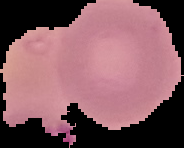

{
  "preparation": "thin blood film",
  "result": "no malaria parasites detected",
  "image_size": "184×148 pixels",
  "image_type": "segmented cell region with the area outside set to black"
}